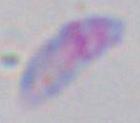
modality = micrograph
magnification = 1000x
identification = Toxoplasma gondii